Report the malaria status of this cell.
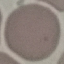

Uninfected.

Summary:
  - Image type: cell patch, automatically extracted from a larger field of view and resized to 64 × 64 pixels
  - Capture: smartphone through the microscope eyepiece
  - Stain: Giemsa
  - Preparation: thin blood smear